Classify this cell by malaria status.
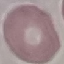

It is uninfected.

Thin blood smear. Cell patch, automatically extracted from a larger field of view and resized to 64 × 64 pixels. Giemsa stain. Photographed with a smartphone camera at the microscope eyepiece.